Assess this cell for malaria.
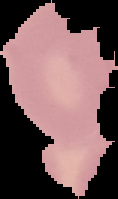
Uninfected.

image type = cell region segmented out of the field of view; surrounding area masked to black
preparation = thin blood film
image size = 118×199 pixels